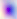

Toxoplasma gondii is shown. Captured at 400x magnification. Photomicrograph.